Locate every Plasmodium falciparum-infected red blood cell.
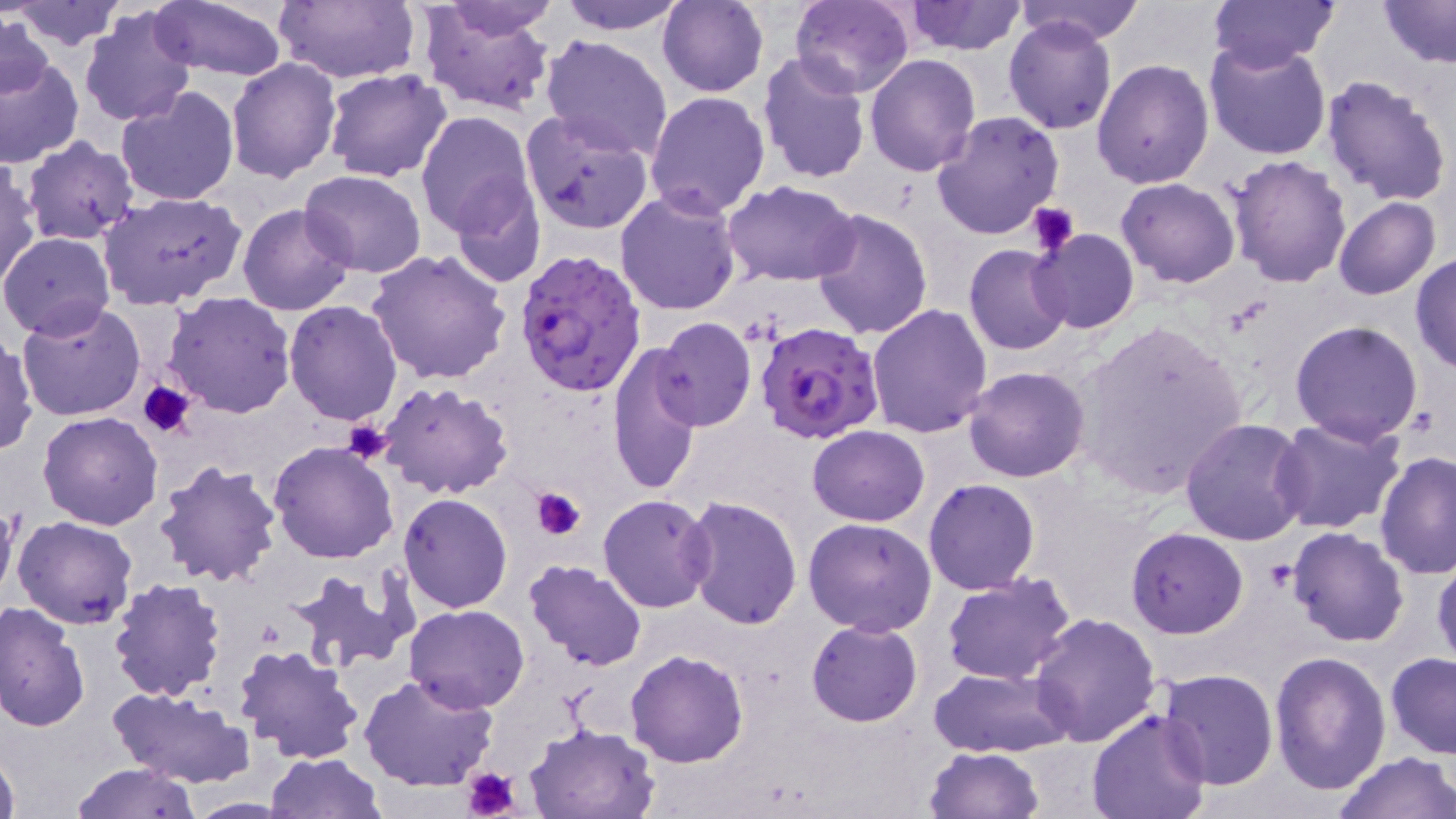

Approximate bounding boxes as [x1, y1, x2, y2] in pixels.
Plasmodium falciparum-infected red blood cells: [515, 248, 648, 398], [755, 322, 885, 444].

slide_level_diagnosis: Plasmodium falciparum
image_size: 1456×819 pixels
field_of_view: one of a larger specimen
preparation: thin blood smear
uninfected_red_blood_cell_locations: 'approximate bounding boxes as [x1, y1, x2, y2] in pixels: [147, 0, 290, 82], [438, 0, 562, 38], [554, 0, 692, 35], [791, 0, 914, 98], [1206, 0, 1340, 72], [1375, 0, 1456, 68], [11, 1, 127, 50], [273, 1, 421, 85], [658, 1, 769, 97], [905, 1, 1027, 55], [1014, 1, 1145, 45], [419, 4, 553, 116], [78, 8, 198, 129], [1, 12, 53, 102], [1004, 17, 1117, 135], [540, 33, 673, 159], [1203, 38, 1332, 160], [0, 50, 83, 169], [756, 53, 871, 184], [865, 53, 981, 175], [227, 57, 341, 184], [1093, 59, 1214, 189], [323, 68, 452, 181], [1322, 74, 1453, 207], [116, 85, 238, 206], [644, 91, 771, 218], [415, 109, 538, 241], [521, 110, 654, 234], [932, 112, 1064, 239], [20, 136, 139, 244], [1227, 154, 1353, 288], [0, 159, 39, 294], [299, 169, 428, 277], [1116, 177, 1239, 288], [723, 180, 859, 288], [449, 183, 547, 288], [616, 188, 743, 315], [97, 192, 247, 311], [1334, 197, 1440, 300], [238, 203, 354, 315], [809, 207, 931, 341], [1030, 228, 1140, 334], [0, 232, 116, 339], [964, 243, 1075, 356], [365, 249, 511, 384], [1411, 253, 1456, 374], [163, 292, 296, 419], [284, 300, 401, 425], [17, 301, 144, 422], [865, 303, 993, 438], [653, 317, 756, 432], [1070, 318, 1248, 499], [1289, 320, 1425, 446], [0, 331, 36, 457], [608, 344, 703, 494], [963, 366, 1091, 482], [378, 382, 515, 499], [38, 411, 164, 529], [1269, 415, 1407, 536], [1179, 418, 1311, 545], [807, 425, 928, 526], [268, 441, 399, 565], [1375, 451, 1456, 578], [152, 459, 284, 588], [924, 478, 1041, 595], [398, 494, 512, 614], [597, 494, 715, 614], [0, 495, 20, 611], [681, 495, 801, 631], [12, 516, 139, 630], [803, 517, 936, 637], [1127, 527, 1248, 638], [1287, 527, 1411, 646], [1431, 554, 1456, 673], [526, 560, 647, 671], [283, 567, 414, 676], [940, 574, 1078, 686], [108, 576, 228, 701], [0, 601, 90, 735], [404, 604, 530, 712], [1029, 611, 1160, 747], [807, 619, 923, 727], [234, 644, 366, 765], [625, 649, 748, 768], [1270, 651, 1392, 797], [1385, 651, 1456, 760], [928, 666, 1073, 758], [1156, 669, 1279, 791], [358, 672, 499, 792], [109, 688, 252, 786], [1088, 709, 1212, 819], [525, 722, 660, 818], [922, 747, 1044, 819], [0, 748, 20, 819], [1336, 752, 1455, 819], [264, 753, 383, 818], [69, 761, 202, 818], [177, 797, 304, 818]'
magnification: 1000x
stain: May-Grünwald-Giemsa
platelet_locations: 'approximate bounding boxes as [x1, y1, x2, y2] in pixels: [1024, 201, 1080, 256], [139, 380, 199, 438], [343, 419, 394, 466], [530, 485, 586, 541], [1263, 561, 1298, 592], [461, 764, 524, 819]'
modality: optical microscopy